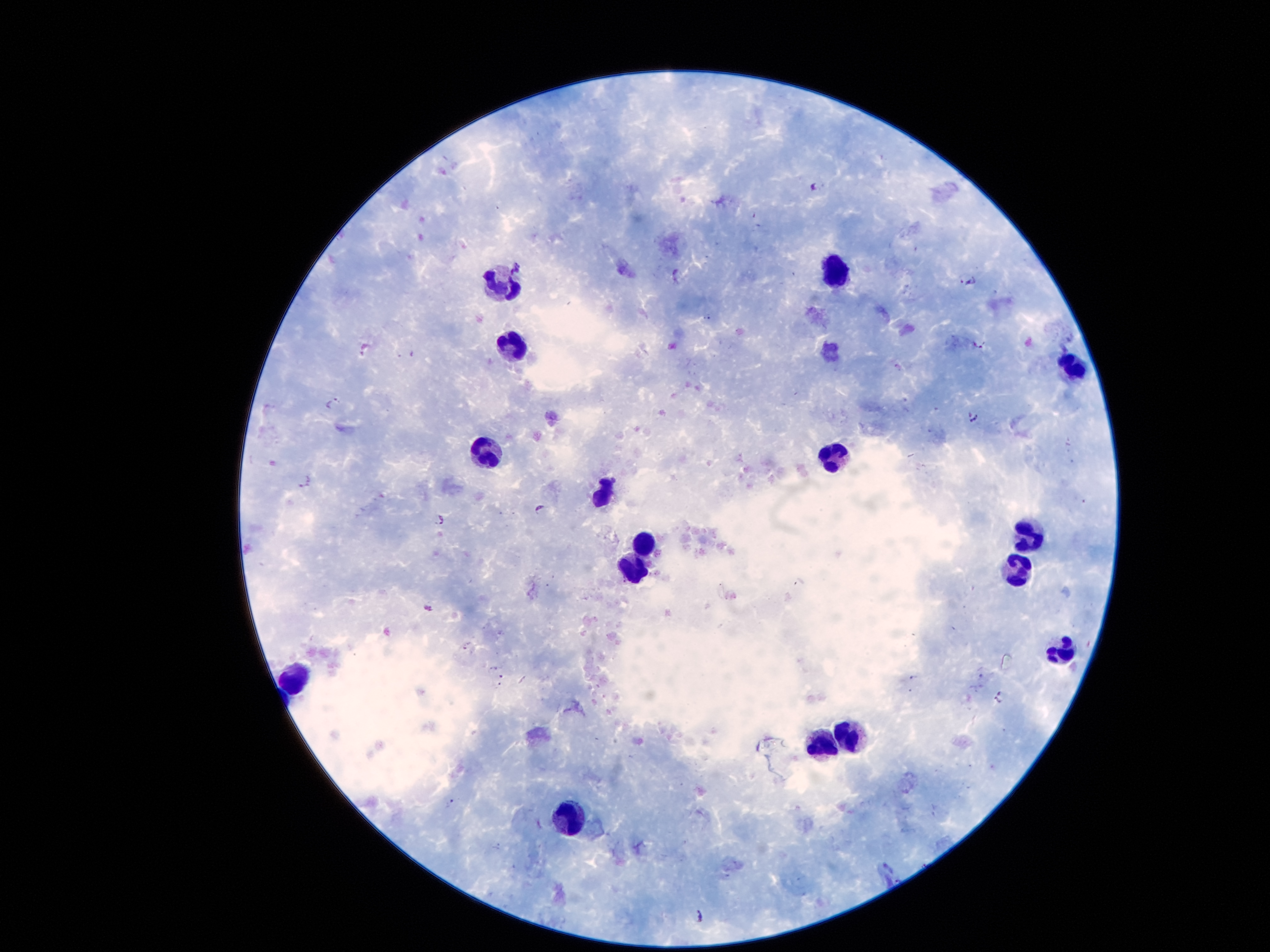

Approximate centers as (x, y) in pixels. Malaria parasite locations: (819, 185), (754, 215), (679, 275), (968, 279), (707, 316), (977, 345), (366, 347), (332, 401), (974, 417), (304, 482), (540, 508), (439, 518), (427, 608), (468, 646), (493, 669), (502, 676), (913, 677), (498, 685), (998, 698), (450, 801), (498, 846), (699, 917). Leukocyte locations: (835, 270), (504, 281), (510, 347), (1072, 363), (486, 453), (831, 454), (605, 494), (1028, 539), (643, 547), (634, 566), (1017, 567), (1061, 652), (298, 673), (855, 737), (824, 746), (572, 819). Giemsa stain. Patient malaria status: positive for Plasmodium falciparum. One field from this slide. 100x magnification. Photographed through the microscope eyepiece with a smartphone camera. Thick peripheral-blood smear. Image is 1270×952 pixels.